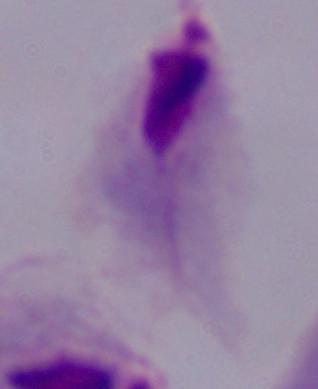 Micrograph. A trichomonad is shown. Captured at 1000x magnification.